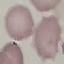 Result: no malaria parasites detected. Thin blood smear. Automatically extracted cell patch, resized to 64 × 64 pixels. Acquired by smartphone through the microscope eyepiece. Giemsa stain.